Assess this cell for malaria.
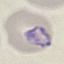

It is parasitized.

Summary:
  - Preparation: thin smear
  - Stain: Giemsa
  - Image type: cell patch, automatically extracted from a larger field of view and resized to 64 × 64 pixels
  - Capture: smartphone camera at the microscope eyepiece